Point out each Plasmodium parasite.
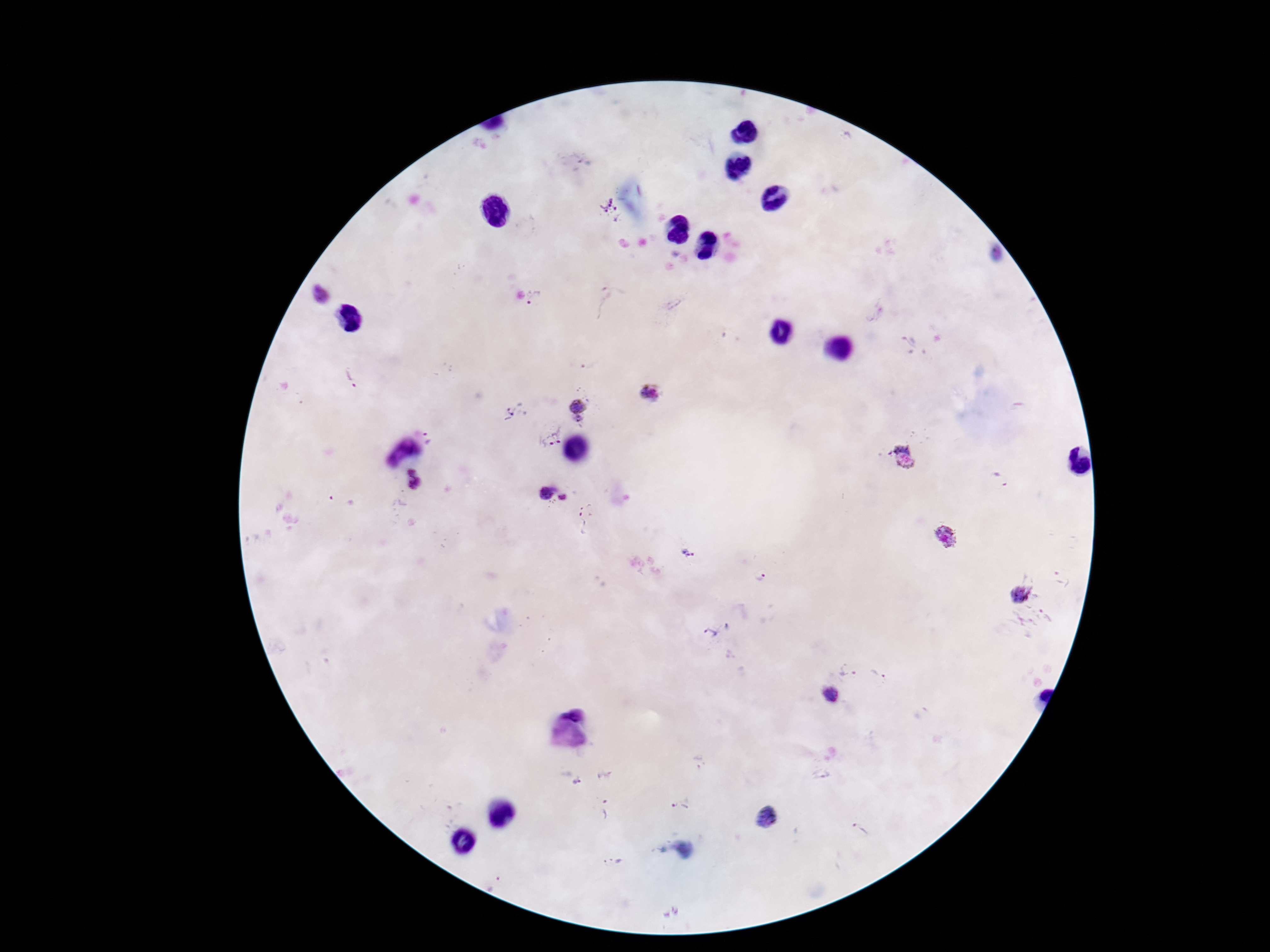

Approximate object centers, in pixels from the top-left corner.
Plasmodium parasites: (x=611, y=211), (x=321, y=294), (x=535, y=298), (x=603, y=303), (x=910, y=344), (x=348, y=383), (x=651, y=392), (x=577, y=405), (x=509, y=412), (x=578, y=420), (x=552, y=435), (x=430, y=437), (x=402, y=451), (x=905, y=460), (x=413, y=479), (x=1001, y=480), (x=547, y=493), (x=563, y=497), (x=342, y=501), (x=586, y=502), (x=585, y=524), (x=947, y=538), (x=686, y=552), (x=760, y=577), (x=1019, y=594), (x=728, y=626), (x=709, y=634), (x=847, y=669), (x=880, y=675), (x=831, y=695), (x=699, y=761), (x=821, y=776), (x=576, y=783), (x=680, y=806), (x=605, y=809), (x=770, y=818), (x=861, y=830), (x=614, y=861), (x=494, y=884).

stain: Giemsa
preparation: thick blood film
patient_malaria_status: positive
field_of_view: single
magnification: 100x
image_size: 1270×952 pixels
capture: smartphone camera through the microscope eyepiece